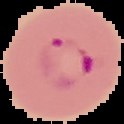
Summary:
  - Image size: 124×124 pixels
  - Preparation: thin blood film
  - Image type: segmented cell region on a black background
  - Result: Plasmodium parasites detected